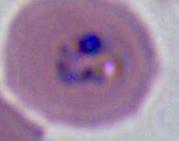
A Plasmodium parasite is shown. 400x or 1000x magnification. Micrograph.